Classify this cell by malaria status.
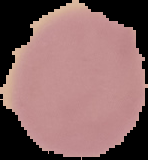

It is uninfected.

Summary:
  - Preparation: thin blood film
  - Image size: 148×160 pixels
  - Image type: segmented cell region on a black background